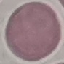

Summary:
  - Result: negative for malaria parasites
  - Capture: smartphone camera at the microscope eyepiece
  - Preparation: thin blood film
  - Stain: Giemsa
  - Image type: automatically extracted cell patch, resized to 64 × 64 pixels